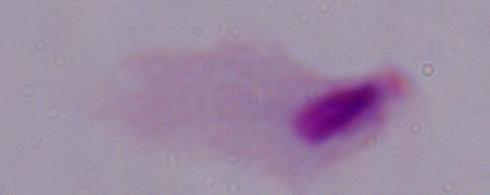

Summary:
  - Magnification: 1000x
  - Modality: micrograph
  - Identification: trichomonad